Comment on the morphology of the red blood cells.
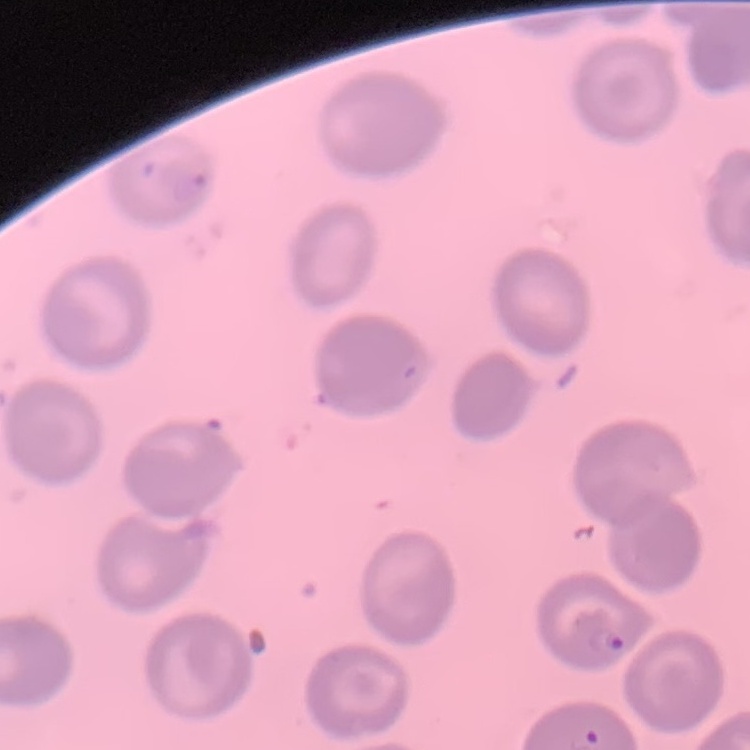
No rouleaux formation.

Stained with either Field's or Giemsa. Square crop of a larger photomicrograph. Thin blood smear.